Identify the blood parasite species.
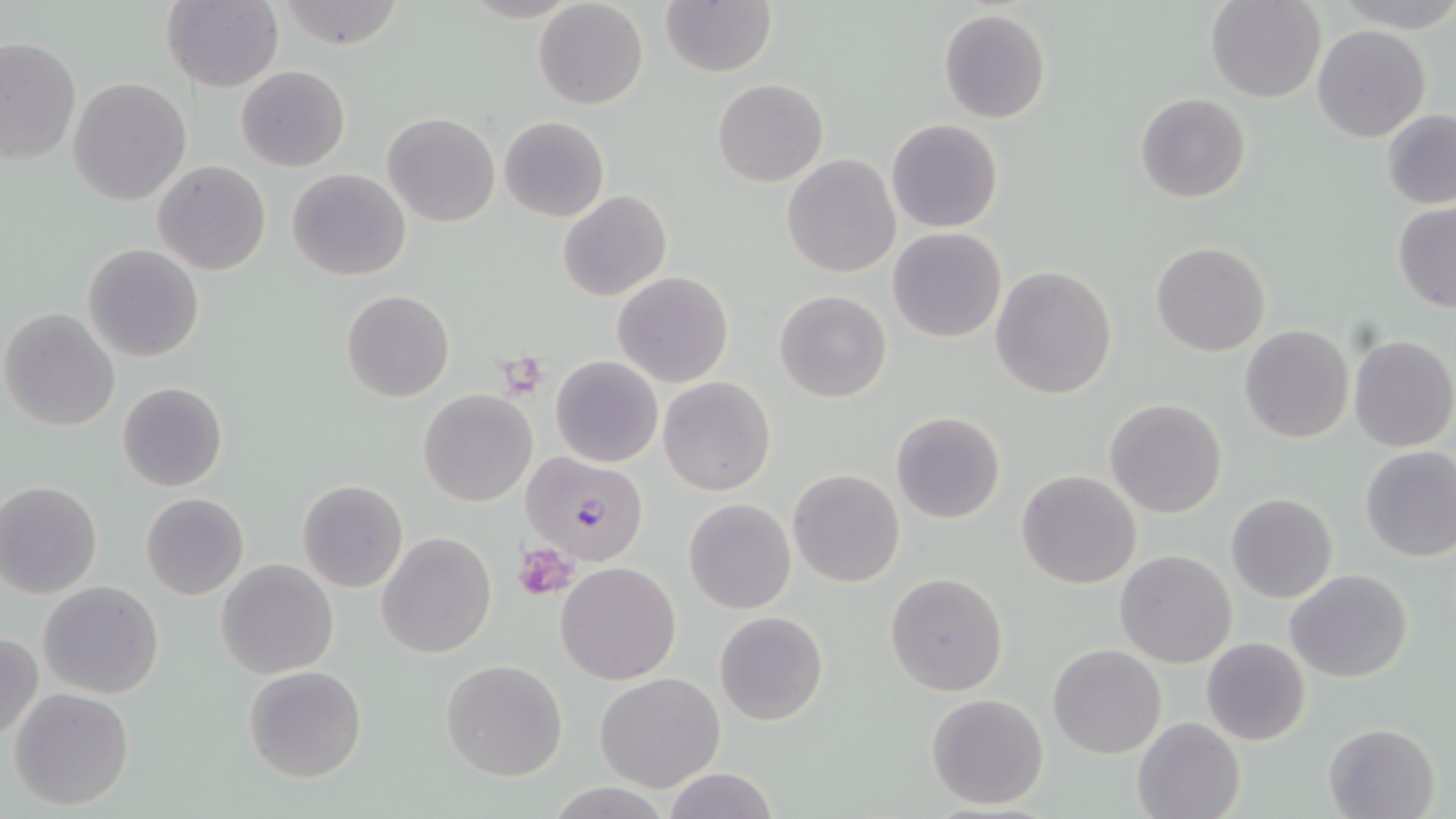
Plasmodium falciparum.

Approximate bounding boxes as (x1, y1, x2, y2) in pixels. Uninfected red blood cell locations: (161, 0, 283, 92), (276, 0, 407, 49), (533, 1, 649, 110), (662, 1, 775, 77), (1205, 1, 1325, 102), (937, 9, 1052, 124), (1312, 25, 1431, 144), (0, 36, 82, 169), (236, 65, 350, 171), (68, 77, 192, 206), (712, 79, 827, 186), (1136, 93, 1251, 204), (1381, 109, 1456, 210), (384, 112, 499, 227), (498, 116, 609, 222), (886, 118, 1004, 233), (783, 154, 899, 277), (152, 160, 271, 275), (286, 168, 411, 281), (558, 190, 671, 302), (1393, 203, 1456, 311), (887, 227, 1007, 343), (1151, 241, 1271, 356), (83, 244, 203, 363), (989, 264, 1117, 400), (613, 271, 733, 388), (341, 290, 455, 403), (774, 290, 892, 403), (0, 309, 120, 431), (1238, 325, 1355, 443), (1348, 335, 1456, 452), (551, 356, 662, 467), (658, 376, 776, 495), (118, 381, 227, 492), (419, 390, 538, 508), (1104, 398, 1228, 519), (891, 411, 1006, 524), (1358, 446, 1456, 563), (789, 469, 904, 587), (1016, 469, 1142, 589), (297, 479, 409, 593), (0, 481, 103, 598), (141, 492, 248, 599), (1226, 493, 1338, 603), (682, 498, 797, 615), (376, 530, 496, 659), (1114, 549, 1237, 667), (216, 558, 340, 679), (555, 562, 681, 685), (1285, 567, 1415, 684), (885, 571, 1009, 696), (39, 581, 163, 698), (715, 611, 829, 726), (0, 633, 44, 743), (1201, 637, 1312, 746), (1048, 644, 1165, 758), (440, 659, 568, 781), (243, 665, 368, 782), (594, 673, 726, 793), (9, 688, 133, 810), (925, 693, 1050, 811), (1132, 716, 1244, 819), (1322, 722, 1440, 819), (660, 766, 779, 819). Plasmodium falciparum-infected red blood cell locations: (522, 451, 652, 565). Platelet locations: (500, 346, 546, 395), (516, 541, 576, 601). May-Grünwald-Giemsa stain. Image is 1456×819 pixels. One field of a larger specimen. Optical microscopy. Thin blood smear. Captured at 1000x magnification.